Comment on the morphology of the red blood cells.
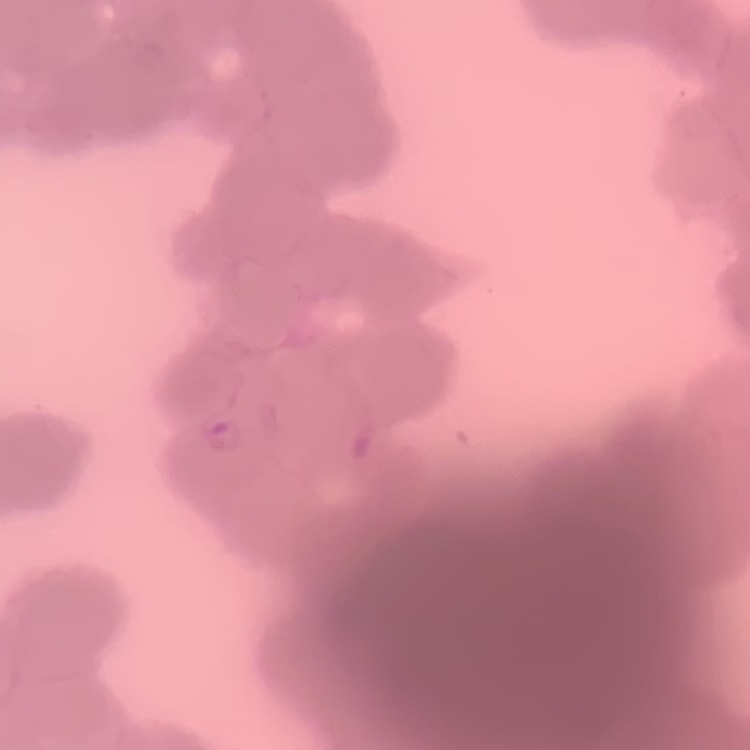
They show rouleaux formation.

preparation = thin peripheral smear
image type = square crop of a larger photomicrograph
stain = Field's or Giemsa